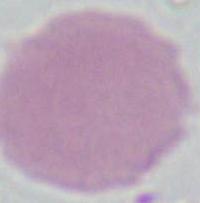

modality = photomicrograph
identification = erythrocyte
magnification = 1000x